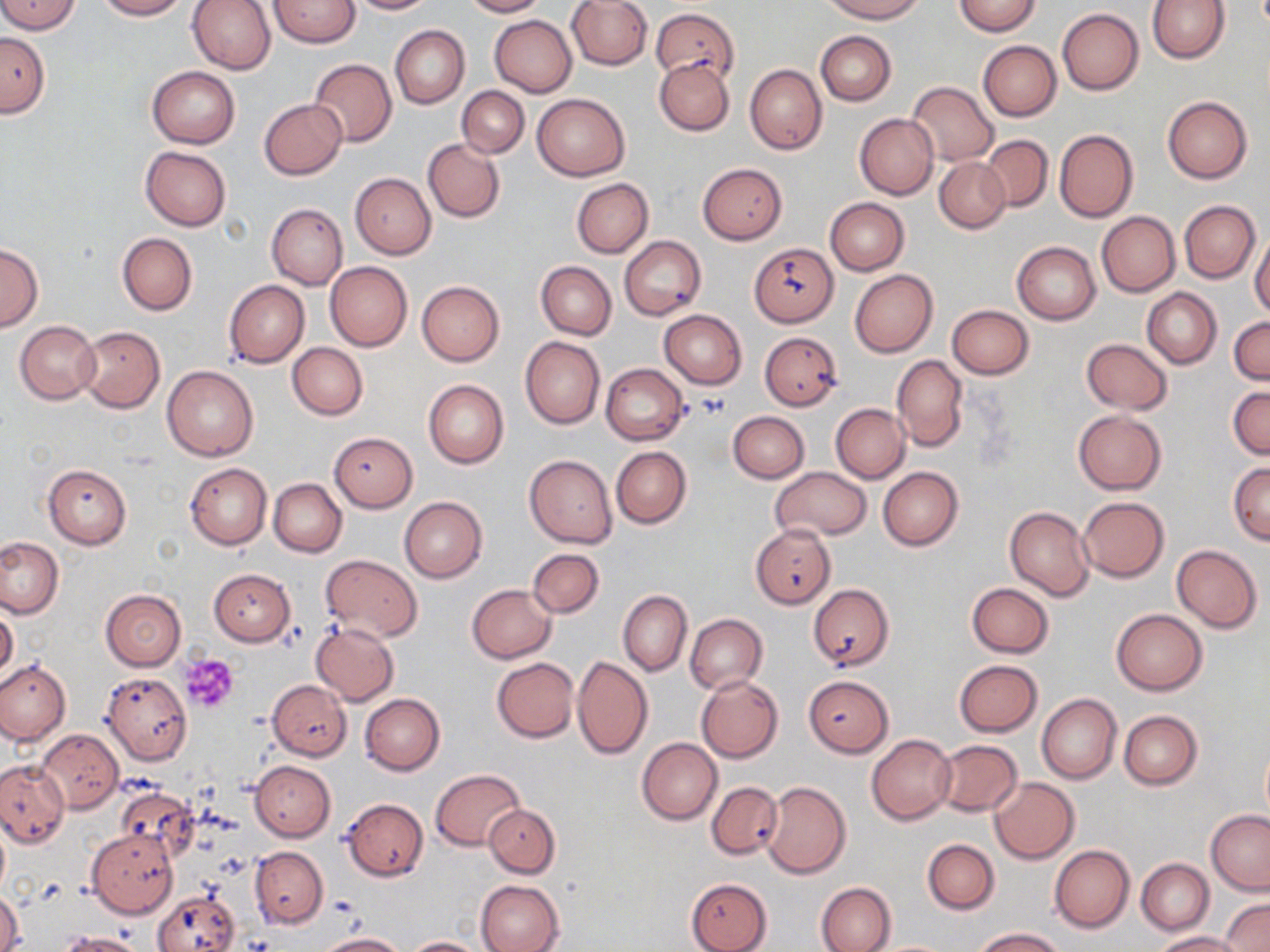
slide_level_diagnosis: no evidence of blood parasites
platelet_locations: 'approximate bounding boxes as (x1, y1, x2, y2) in pixels: (697, 395, 731, 419), (179, 653, 239, 713)'
stain: May-Grünwald-Giemsa
preparation: thin blood smear
modality: optical microscopy
field_of_view: single
magnification: 1000x
uninfected_red_blood_cell_locations: 'approximate bounding boxes as (x1, y1, x2, y2) in pixels: (0, 0, 81, 34), (94, 0, 188, 20), (187, 0, 275, 74), (269, 0, 360, 47), (346, 0, 434, 14), (462, 0, 546, 17), (566, 0, 651, 71), (824, 0, 924, 22), (1148, 0, 1230, 64), (954, 1, 1042, 36), (652, 8, 738, 84), (1057, 8, 1143, 95), (489, 15, 577, 97), (390, 25, 470, 108), (815, 31, 895, 106), (0, 32, 50, 116), (978, 40, 1061, 121), (655, 57, 735, 135), (309, 58, 396, 147), (745, 64, 828, 155), (148, 66, 239, 148), (907, 81, 1000, 166), (456, 86, 529, 158), (531, 92, 630, 181), (1163, 96, 1252, 183), (259, 98, 347, 179), (854, 113, 938, 199), (1054, 129, 1138, 222), (981, 135, 1052, 212), (423, 139, 505, 222), (140, 146, 231, 230), (934, 157, 1010, 232), (697, 162, 787, 244), (350, 173, 436, 258), (572, 178, 653, 258), (825, 197, 909, 275), (1179, 200, 1259, 283), (267, 204, 347, 290), (1097, 211, 1180, 296), (117, 233, 196, 315), (1250, 234, 1270, 318), (620, 236, 706, 320), (1012, 241, 1101, 324), (750, 242, 839, 327), (0, 244, 43, 333), (325, 261, 412, 351), (536, 261, 616, 340), (849, 269, 938, 357), (224, 280, 308, 367), (417, 280, 504, 366), (1141, 288, 1222, 369), (946, 304, 1034, 379), (660, 309, 746, 388), (1229, 316, 1270, 384), (14, 321, 100, 404), (78, 326, 164, 412), (759, 331, 843, 411), (520, 336, 605, 430), (1080, 338, 1174, 414), (288, 342, 367, 419), (892, 355, 968, 451), (600, 364, 689, 445), (162, 365, 258, 460), (423, 379, 509, 469), (1228, 384, 1269, 460), (831, 403, 909, 483), (1072, 409, 1167, 495), (728, 411, 808, 484), (329, 432, 418, 512), (610, 446, 692, 529), (524, 455, 617, 548), (185, 462, 271, 549), (1228, 462, 1270, 544), (43, 465, 132, 548), (770, 467, 872, 540), (878, 467, 963, 550), (269, 479, 347, 557), (398, 496, 488, 582), (1077, 497, 1170, 581), (1004, 506, 1094, 601), (751, 523, 836, 609), (0, 536, 64, 619), (1171, 545, 1262, 633), (529, 548, 604, 618), (320, 554, 422, 642), (208, 568, 296, 646), (809, 583, 894, 671), (966, 583, 1055, 659), (468, 585, 556, 663), (101, 589, 186, 672), (618, 591, 692, 676), (0, 607, 19, 682), (1112, 608, 1207, 694), (686, 614, 767, 695), (311, 622, 398, 706), (572, 655, 653, 759), (492, 658, 579, 742), (1, 659, 70, 746), (955, 659, 1042, 736), (102, 672, 192, 764), (696, 675, 784, 763), (803, 675, 895, 757), (267, 679, 352, 760), (359, 693, 444, 776), (1037, 693, 1122, 785), (1119, 711, 1203, 790), (38, 729, 123, 813), (867, 734, 956, 825), (1260, 737, 1270, 826), (637, 738, 722, 824), (933, 739, 1023, 817), (0, 760, 69, 847), (250, 760, 336, 841), (431, 769, 524, 851), (989, 777, 1080, 864), (759, 780, 851, 878), (706, 781, 783, 858), (115, 785, 196, 862), (342, 798, 428, 881), (484, 802, 559, 878), (1206, 810, 1270, 895), (0, 820, 9, 896), (87, 827, 179, 918), (922, 839, 999, 914), (1049, 845, 1135, 932), (250, 847, 327, 928), (1136, 858, 1213, 935), (685, 877, 772, 952), (476, 879, 563, 952), (816, 881, 896, 952), (1, 888, 23, 952), (153, 889, 241, 951), (1222, 898, 1270, 951), (974, 928, 1066, 951), (59, 931, 147, 952), (1152, 931, 1247, 951), (314, 932, 409, 951), (405, 935, 486, 951)'
image_size: 1270×952 pixels